Mark where leukocytes are.
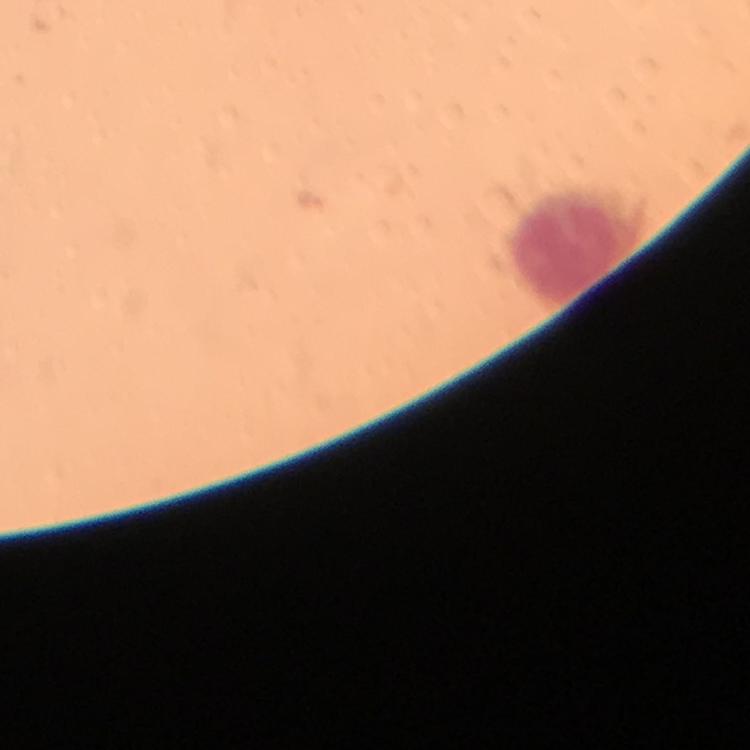
Approximate centers as (x, y) in pixels.
Leukocytes: (570, 248).

stain: Giemsa
capture: smartphone camera through the microscope
immersion_oil: used
magnification: 100x
context: from a diagnostic examination for malaria
image_size: 750×750 pixels
plasmodium_parasites: none seen
preparation: thick smear
cropped_from: one field of view